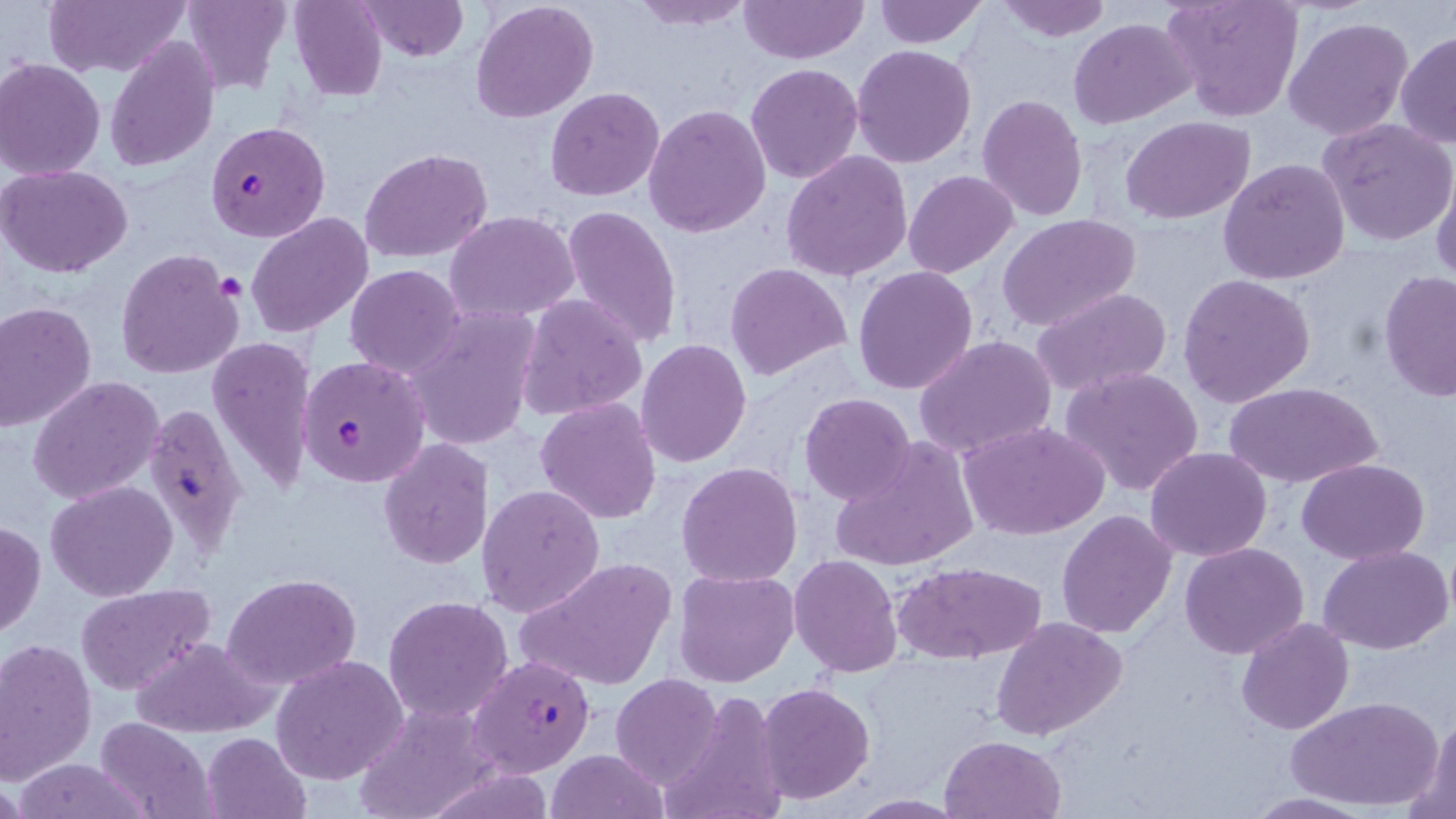

Summary:
  - Coordinate format: approximate bounding boxes as (x1,y1)-(x2,y2) corner pairs in pixels
  - Platelet locations: (214,276)-(246,301)
  - Plasmodium falciparum-infected red blood cell locations: (206,120)-(330,242), (297,354)-(428,487), (142,402)-(249,559), (468,653)-(597,780)
  - Uninfected red blood cell locations: (44,0)-(190,77), (181,0)-(291,92), (289,0)-(387,101), (359,0)-(468,60), (470,0)-(599,122), (627,0)-(754,30), (739,0)-(868,63), (873,0)-(988,47), (993,0)-(1112,40), (1161,0)-(1304,122), (1284,16)-(1414,141), (1070,20)-(1193,130), (1396,32)-(1456,148), (103,37)-(219,173), (852,44)-(977,168), (0,58)-(105,178), (746,62)-(864,184), (545,86)-(665,202), (978,95)-(1087,221), (644,104)-(771,237), (1120,117)-(1255,224), (1318,118)-(1456,247), (359,148)-(493,261), (782,151)-(913,282), (1219,159)-(1351,284), (1431,161)-(1455,286), (0,164)-(134,278), (903,170)-(1019,277), (560,204)-(683,351), (447,210)-(581,322), (246,212)-(373,339), (999,215)-(1140,333), (114,247)-(243,380), (725,263)-(852,381), (344,264)-(466,379), (853,265)-(978,395), (1379,270)-(1456,405), (1177,274)-(1317,408), (1030,286)-(1172,399), (518,294)-(647,422), (0,302)-(97,432), (405,310)-(540,451), (915,334)-(1059,459), (208,337)-(317,496), (637,337)-(753,468), (1063,366)-(1205,497), (29,375)-(166,503), (1225,381)-(1380,489), (799,393)-(916,504), (536,397)-(661,523), (958,420)-(1110,540), (378,438)-(494,569), (829,440)-(979,572), (1145,447)-(1273,561), (1297,459)-(1428,564), (677,461)-(803,587), (46,482)-(178,602), (476,483)-(605,617), (1057,510)-(1177,640), (0,520)-(46,640), (1180,543)-(1310,659), (1320,543)-(1453,654), (788,555)-(903,676), (517,557)-(676,692), (895,561)-(1047,662), (674,569)-(799,688), (224,572)-(361,689), (75,584)-(217,697), (382,595)-(514,723), (1236,616)-(1355,735), (994,617)-(1125,740), (130,636)-(274,736), (0,638)-(98,784), (271,655)-(407,785), (612,673)-(721,786), (757,682)-(874,803), (656,691)-(788,819), (1287,697)-(1442,811), (353,702)-(497,819), (1417,709)-(1454,819), (94,718)-(218,818), (201,732)-(311,819), (941,734)-(1066,818), (546,748)-(665,819), (11,757)-(153,819), (1239,793)-(1380,819), (844,795)-(971,817)
  - Slide-level diagnosis: Plasmodium falciparum
  - Modality: light microscopy
  - Stain: May-Grünwald-Giemsa
  - Preparation: thin blood film
  - Field of view: one of a larger specimen
  - Image size: 1456×819 pixels
  - Magnification: 1000x